Assess this cell for malaria.
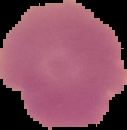
It is uninfected.

Summary:
  - Preparation: thin blood smear
  - Image type: segmented cell region with the area outside set to black
  - Image size: 127×130 pixels